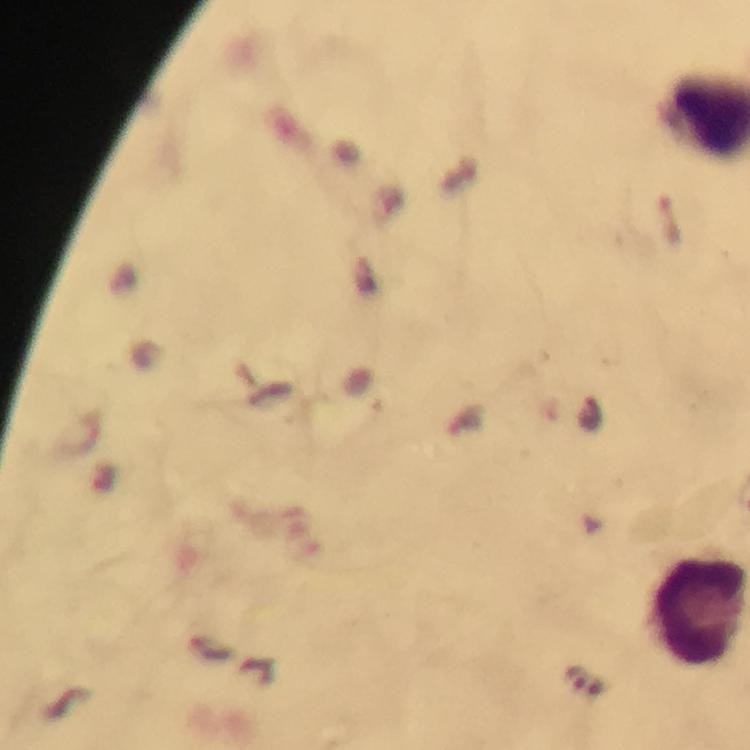
Approximate centers as (x, y) in pixels.
Summary:
  - Leukocyte locations: (697, 617)
  - Cropped from: a single field of view
  - Context: from a malaria diagnostic workup
  - Image size: 750×750 pixels
  - Malaria parasites: none detected
  - Stain: Giemsa
  - Capture: smartphone photograph through a microscope
  - Immersion oil: used
  - Magnification: 100x
  - Preparation: thick blood smear